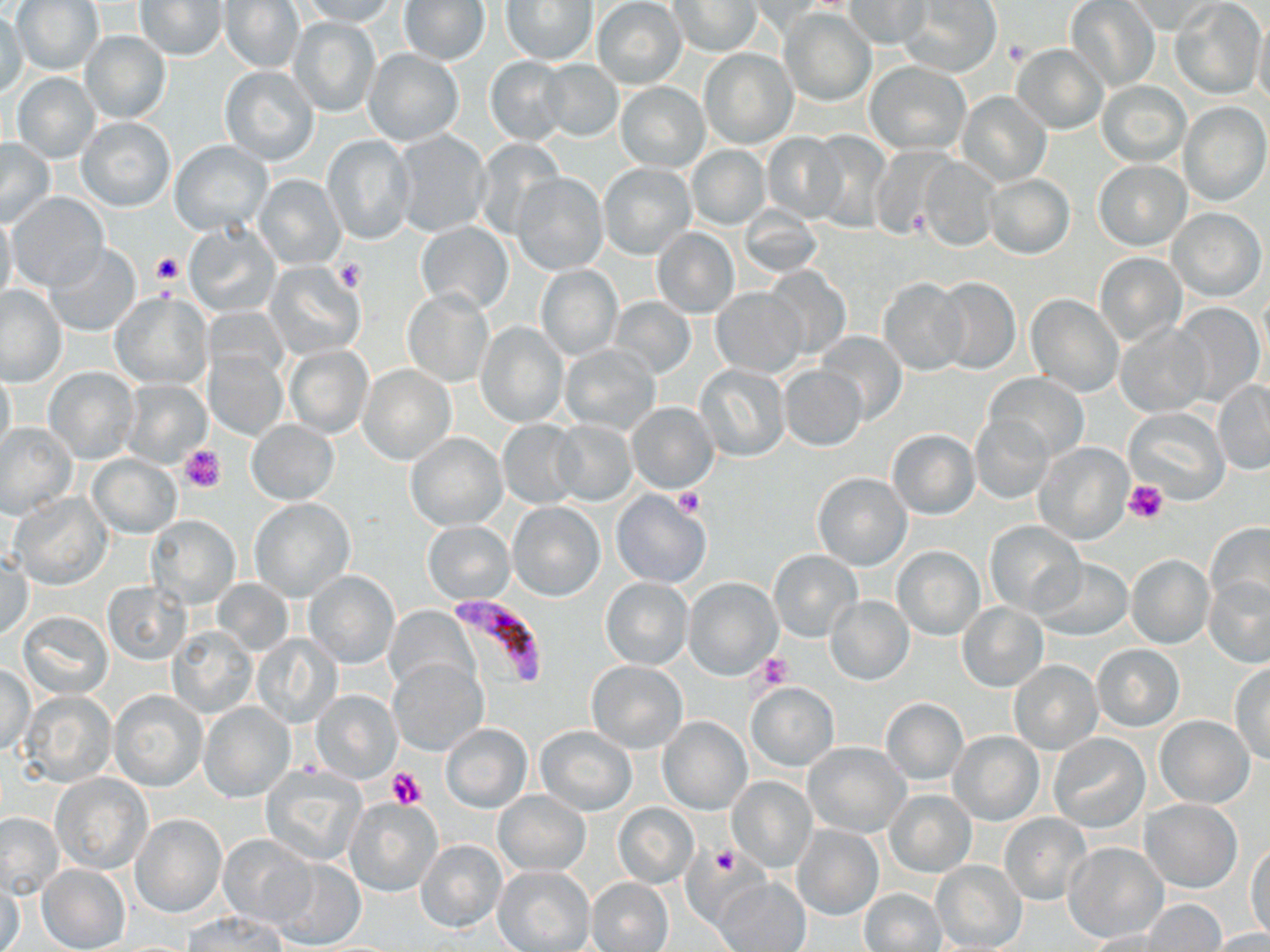
Summary:
  - Coordinate format: approximate bounding boxes as named x1/y1/x2/y2 corners in pixels
  - Plasmodium falciparum-infected red blood cell locations: (x1=452, y1=596, x2=545, y2=690)
  - Platelet locations: (x1=1004, y1=37, x2=1032, y2=65), (x1=151, y1=251, x2=185, y2=286), (x1=335, y1=260, x2=364, y2=292), (x1=178, y1=444, x2=226, y2=495), (x1=1124, y1=480, x2=1169, y2=525), (x1=673, y1=489, x2=704, y2=518), (x1=754, y1=651, x2=792, y2=688), (x1=387, y1=767, x2=428, y2=810), (x1=709, y1=845, x2=742, y2=877)
  - Uninfected red blood cell locations: (x1=12, y1=0, x2=104, y2=76), (x1=222, y1=0, x2=303, y2=73), (x1=298, y1=0, x2=396, y2=25), (x1=898, y1=0, x2=1002, y2=76), (x1=134, y1=1, x2=228, y2=61), (x1=500, y1=1, x2=599, y2=66), (x1=593, y1=1, x2=687, y2=88), (x1=670, y1=1, x2=763, y2=57), (x1=845, y1=1, x2=931, y2=50), (x1=1064, y1=1, x2=1160, y2=91), (x1=1127, y1=1, x2=1220, y2=35), (x1=1171, y1=1, x2=1265, y2=100), (x1=399, y1=2, x2=490, y2=66), (x1=747, y1=2, x2=832, y2=36), (x1=781, y1=8, x2=877, y2=106), (x1=0, y1=9, x2=28, y2=98), (x1=1251, y1=14, x2=1270, y2=110), (x1=288, y1=16, x2=381, y2=118), (x1=79, y1=30, x2=172, y2=124), (x1=1011, y1=43, x2=1108, y2=134), (x1=364, y1=49, x2=464, y2=146), (x1=699, y1=49, x2=797, y2=149), (x1=484, y1=56, x2=571, y2=144), (x1=539, y1=58, x2=625, y2=141), (x1=863, y1=61, x2=970, y2=155), (x1=219, y1=66, x2=320, y2=165), (x1=11, y1=72, x2=101, y2=161), (x1=1097, y1=80, x2=1192, y2=167), (x1=614, y1=81, x2=710, y2=171), (x1=957, y1=90, x2=1051, y2=186), (x1=1179, y1=101, x2=1269, y2=206), (x1=75, y1=116, x2=175, y2=212), (x1=388, y1=129, x2=493, y2=239), (x1=806, y1=130, x2=892, y2=228), (x1=762, y1=133, x2=846, y2=222), (x1=322, y1=135, x2=415, y2=245), (x1=0, y1=138, x2=56, y2=227), (x1=473, y1=138, x2=565, y2=239), (x1=168, y1=139, x2=274, y2=236), (x1=686, y1=144, x2=770, y2=230), (x1=870, y1=144, x2=956, y2=242), (x1=919, y1=156, x2=1001, y2=252), (x1=1093, y1=161, x2=1190, y2=251), (x1=598, y1=162, x2=696, y2=259), (x1=512, y1=172, x2=608, y2=276), (x1=983, y1=174, x2=1074, y2=261), (x1=254, y1=175, x2=345, y2=268), (x1=8, y1=194, x2=109, y2=292), (x1=740, y1=204, x2=823, y2=279), (x1=1168, y1=208, x2=1265, y2=300), (x1=0, y1=211, x2=17, y2=307), (x1=415, y1=221, x2=513, y2=314), (x1=183, y1=222, x2=281, y2=316), (x1=651, y1=227, x2=739, y2=319), (x1=44, y1=245, x2=143, y2=337), (x1=1093, y1=253, x2=1186, y2=347), (x1=265, y1=261, x2=366, y2=360), (x1=536, y1=265, x2=622, y2=361), (x1=761, y1=267, x2=850, y2=361), (x1=932, y1=276, x2=1021, y2=375), (x1=878, y1=278, x2=969, y2=375), (x1=0, y1=286, x2=66, y2=386), (x1=711, y1=287, x2=804, y2=376), (x1=402, y1=290, x2=493, y2=387), (x1=109, y1=291, x2=211, y2=389), (x1=1026, y1=295, x2=1123, y2=396), (x1=609, y1=297, x2=696, y2=378), (x1=1169, y1=301, x2=1266, y2=406), (x1=1115, y1=321, x2=1211, y2=417), (x1=475, y1=322, x2=569, y2=427), (x1=816, y1=333, x2=907, y2=424), (x1=284, y1=344, x2=374, y2=438), (x1=559, y1=344, x2=661, y2=434), (x1=205, y1=349, x2=286, y2=440), (x1=695, y1=364, x2=790, y2=461), (x1=357, y1=365, x2=457, y2=467), (x1=778, y1=365, x2=868, y2=452), (x1=0, y1=366, x2=16, y2=461), (x1=44, y1=368, x2=139, y2=463), (x1=984, y1=373, x2=1089, y2=461), (x1=122, y1=380, x2=211, y2=468), (x1=1213, y1=380, x2=1270, y2=475), (x1=626, y1=401, x2=719, y2=494), (x1=1123, y1=405, x2=1230, y2=505), (x1=970, y1=413, x2=1056, y2=502), (x1=246, y1=420, x2=339, y2=504), (x1=497, y1=420, x2=582, y2=508), (x1=551, y1=420, x2=637, y2=506), (x1=0, y1=422, x2=77, y2=520), (x1=887, y1=430, x2=980, y2=519), (x1=405, y1=432, x2=506, y2=530), (x1=1033, y1=442, x2=1133, y2=545), (x1=88, y1=454, x2=180, y2=537), (x1=812, y1=472, x2=912, y2=571), (x1=610, y1=490, x2=711, y2=589), (x1=8, y1=493, x2=112, y2=590), (x1=250, y1=498, x2=356, y2=601), (x1=508, y1=503, x2=605, y2=601), (x1=146, y1=514, x2=240, y2=609), (x1=423, y1=521, x2=513, y2=602), (x1=985, y1=521, x2=1086, y2=617), (x1=1204, y1=523, x2=1269, y2=613), (x1=893, y1=545, x2=985, y2=640), (x1=768, y1=549, x2=861, y2=642), (x1=1125, y1=554, x2=1214, y2=649), (x1=1, y1=556, x2=34, y2=639), (x1=1032, y1=558, x2=1133, y2=641), (x1=303, y1=571, x2=400, y2=668), (x1=1204, y1=576, x2=1270, y2=668), (x1=600, y1=577, x2=693, y2=668), (x1=684, y1=578, x2=781, y2=681), (x1=212, y1=580, x2=294, y2=657), (x1=101, y1=581, x2=190, y2=664), (x1=825, y1=595, x2=914, y2=686), (x1=958, y1=602, x2=1049, y2=692), (x1=387, y1=607, x2=476, y2=695), (x1=18, y1=611, x2=113, y2=699), (x1=168, y1=627, x2=256, y2=718), (x1=253, y1=633, x2=341, y2=729), (x1=1092, y1=644, x2=1184, y2=731), (x1=389, y1=659, x2=488, y2=755), (x1=585, y1=660, x2=688, y2=754), (x1=1007, y1=660, x2=1103, y2=754), (x1=1230, y1=662, x2=1270, y2=763), (x1=0, y1=663, x2=36, y2=756), (x1=744, y1=682, x2=839, y2=771), (x1=108, y1=688, x2=207, y2=791), (x1=311, y1=689, x2=401, y2=784), (x1=21, y1=691, x2=116, y2=788), (x1=879, y1=698, x2=968, y2=785), (x1=199, y1=702, x2=295, y2=802), (x1=1153, y1=714, x2=1255, y2=806), (x1=658, y1=717, x2=752, y2=816), (x1=441, y1=722, x2=532, y2=812), (x1=536, y1=725, x2=636, y2=815), (x1=947, y1=731, x2=1043, y2=825), (x1=1048, y1=733, x2=1151, y2=833), (x1=802, y1=741, x2=910, y2=837), (x1=259, y1=764, x2=366, y2=867), (x1=51, y1=774, x2=153, y2=873), (x1=727, y1=778, x2=816, y2=871), (x1=494, y1=789, x2=590, y2=876), (x1=884, y1=789, x2=976, y2=878), (x1=343, y1=796, x2=442, y2=896), (x1=1141, y1=798, x2=1241, y2=892), (x1=612, y1=803, x2=697, y2=887), (x1=1, y1=812, x2=62, y2=900), (x1=998, y1=812, x2=1093, y2=906), (x1=133, y1=815, x2=225, y2=917), (x1=791, y1=825, x2=883, y2=921), (x1=217, y1=832, x2=316, y2=928), (x1=416, y1=839, x2=506, y2=932), (x1=1063, y1=843, x2=1168, y2=943), (x1=1246, y1=843, x2=1269, y2=942), (x1=270, y1=858, x2=366, y2=947), (x1=931, y1=861, x2=1027, y2=951), (x1=38, y1=864, x2=130, y2=952), (x1=494, y1=865, x2=595, y2=952), (x1=715, y1=876, x2=811, y2=952), (x1=586, y1=877, x2=673, y2=952), (x1=1, y1=881, x2=25, y2=952), (x1=861, y1=888, x2=947, y2=951), (x1=1141, y1=899, x2=1227, y2=951), (x1=184, y1=912, x2=285, y2=951), (x1=1083, y1=929, x2=1179, y2=952), (x1=1205, y1=930, x2=1270, y2=951)
  - Slide-level diagnosis: Plasmodium falciparum
  - Image size: 1270×952 pixels
  - Modality: light microscopy
  - Magnification: 1000x
  - Field of view: single
  - Stain: May-Grünwald-Giemsa
  - Preparation: thin blood smear